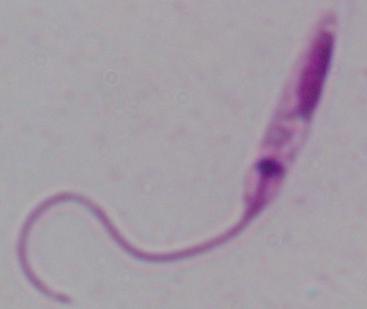

Summary:
  - Magnification: 1000x
  - Modality: photomicrograph
  - Identification: Leishmania